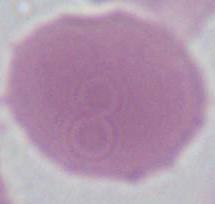
magnification = 1000x
identification = erythrocyte
modality = micrograph